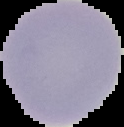

{
  "result": "no Plasmodium parasites seen",
  "image_type": "segmented cell region with the area outside set to black",
  "image_size": "124×127 pixels",
  "preparation": "thin blood film"
}